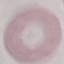

Result: no malaria parasites seen. Thin blood smear. Automatically extracted cell patch, resized to 64 × 64 pixels. Giemsa stain. Photographed with a smartphone camera at the microscope eyepiece.